Identify the preparation type.
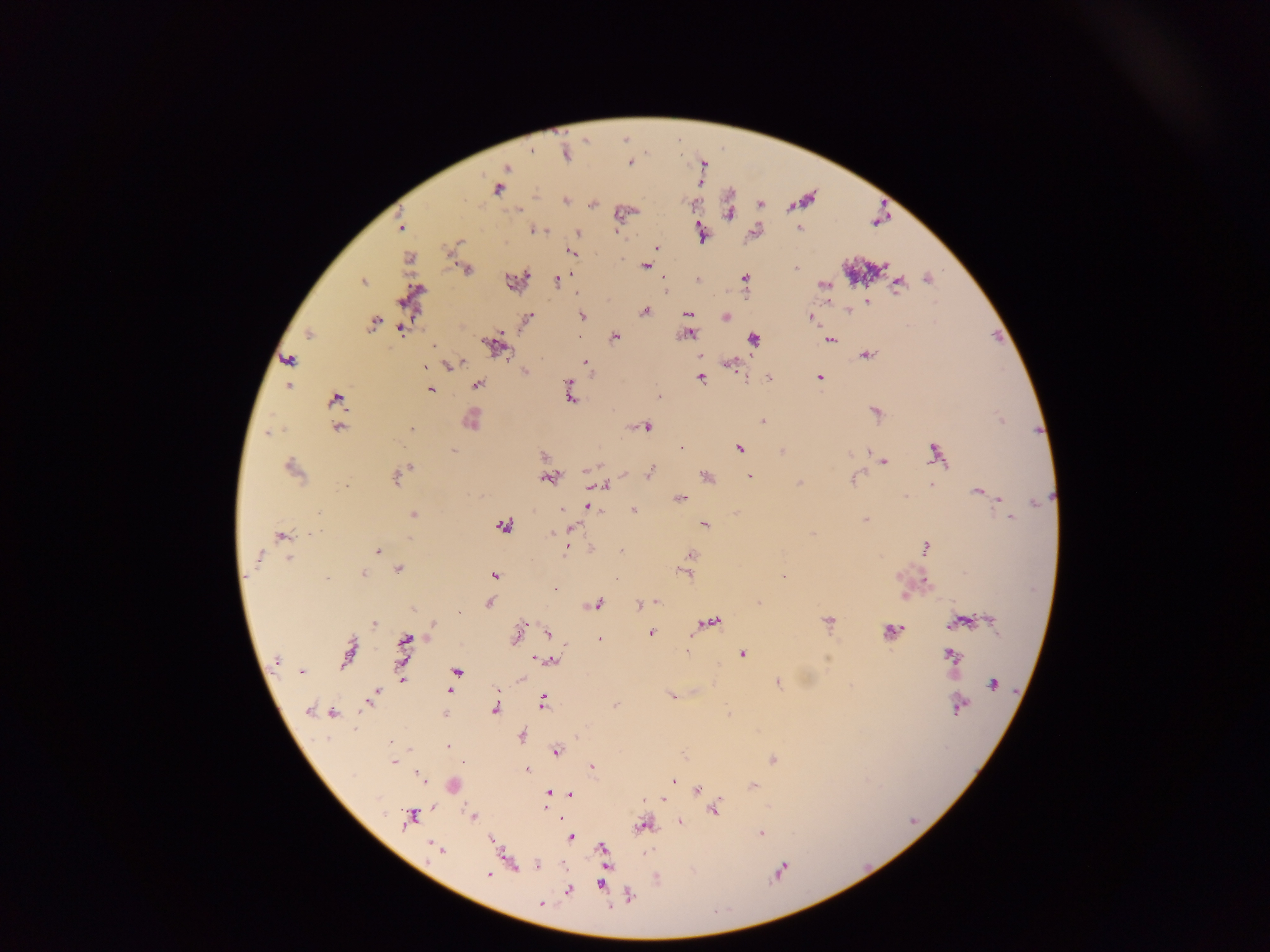
Thick blood smear.

Approximate centers as {x, y} in pixels. Leukocyte locations: {474, 417}, {454, 785}. Plasmodium parasite locations: {531, 150}, {567, 154}, {630, 163}, {507, 167}, {497, 189}, {565, 201}, {760, 203}, {591, 204}, {728, 214}, {399, 227}, {799, 228}, {536, 230}, {578, 232}, {700, 233}, {657, 247}, {570, 252}, {408, 258}, {645, 266}, {883, 266}, {795, 268}, {467, 270}, {527, 276}, {744, 278}, {927, 278}, {698, 279}, {557, 280}, {512, 281}, {363, 282}, {823, 284}, {898, 284}, {867, 301}, {645, 311}, {848, 311}, {688, 314}, {582, 316}, {726, 317}, {528, 318}, {812, 318}, {373, 323}, {401, 330}, {309, 334}, {688, 334}, {615, 337}, {753, 339}, {829, 341}, {433, 346}, {494, 346}, {866, 355}, {288, 360}, {585, 363}, {729, 364}, {424, 366}, {449, 366}, {525, 372}, {819, 377}, {767, 378}, {701, 379}, {477, 385}, {289, 386}, {570, 386}, {430, 389}, {570, 395}, {659, 396}, {335, 399}, {875, 412}, {1001, 420}, {762, 421}, {647, 427}, {338, 428}, {411, 430}, {268, 432}, {681, 448}, {740, 449}, {453, 450}, {782, 451}, {869, 452}, {935, 453}, {544, 455}, {885, 462}, {409, 468}, {292, 469}, {650, 471}, {406, 472}, {706, 476}, {749, 477}, {396, 478}, {549, 478}, {852, 480}, {799, 482}, {930, 485}, {346, 486}, {603, 486}, {977, 492}, {680, 498}, {1000, 500}, {1037, 503}, {589, 507}, {561, 509}, {634, 510}, {414, 515}, {1010, 519}, {865, 520}, {704, 525}, {504, 526}, {571, 529}, {314, 532}, {551, 532}, {812, 534}, {281, 536}, {410, 540}, {925, 546}, {567, 547}, {378, 550}, {621, 550}, {692, 555}, {258, 556}, {290, 559}, {403, 566}, {686, 573}, {364, 574}, {494, 575}, {783, 576}, {327, 578}, {926, 581}, {556, 589}, {904, 595}, {655, 602}, {490, 603}, {759, 603}, {598, 604}, {639, 605}, {458, 612}, {713, 620}, {828, 620}, {992, 621}, {960, 622}, {375, 624}, {432, 625}, {893, 631}, {548, 633}, {651, 633}, {516, 635}, {599, 639}, {407, 640}, {348, 652}, {742, 654}, {951, 655}, {540, 659}, {276, 660}, {550, 661}, {302, 671}, {457, 672}, {402, 678}, {778, 683}, {993, 684}, {450, 692}, {375, 693}, {672, 696}, {543, 702}, {367, 703}, {615, 705}, {958, 707}, {495, 709}, {308, 710}, {333, 713}, {728, 714}, {522, 737}, {392, 744}, {447, 746}, {557, 752}, {773, 760}, {393, 762}, {462, 763}, {592, 768}, {527, 770}, {420, 775}, {673, 781}, {754, 785}, {697, 789}, {548, 793}, {570, 794}, {662, 799}, {546, 801}, {715, 810}, {473, 817}, {409, 818}, {679, 821}, {644, 826}, {760, 833}, {571, 837}, {435, 847}, {602, 848}, {440, 849}, {538, 866}, {780, 871}, {488, 874}, {601, 884}, {569, 890}, {629, 896}, {542, 904}. Sample from Ghana. Mobile-phone photograph taken through the microscope. Image is 1270×952 pixels. One field of view.